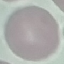
Summary:
  - Malaria status: uninfected
  - Stain: Giemsa
  - Image type: cell patch, automatically extracted from a larger field of view and resized to 64 × 64 pixels
  - Preparation: thin smear
  - Capture: smartphone through the microscope eyepiece